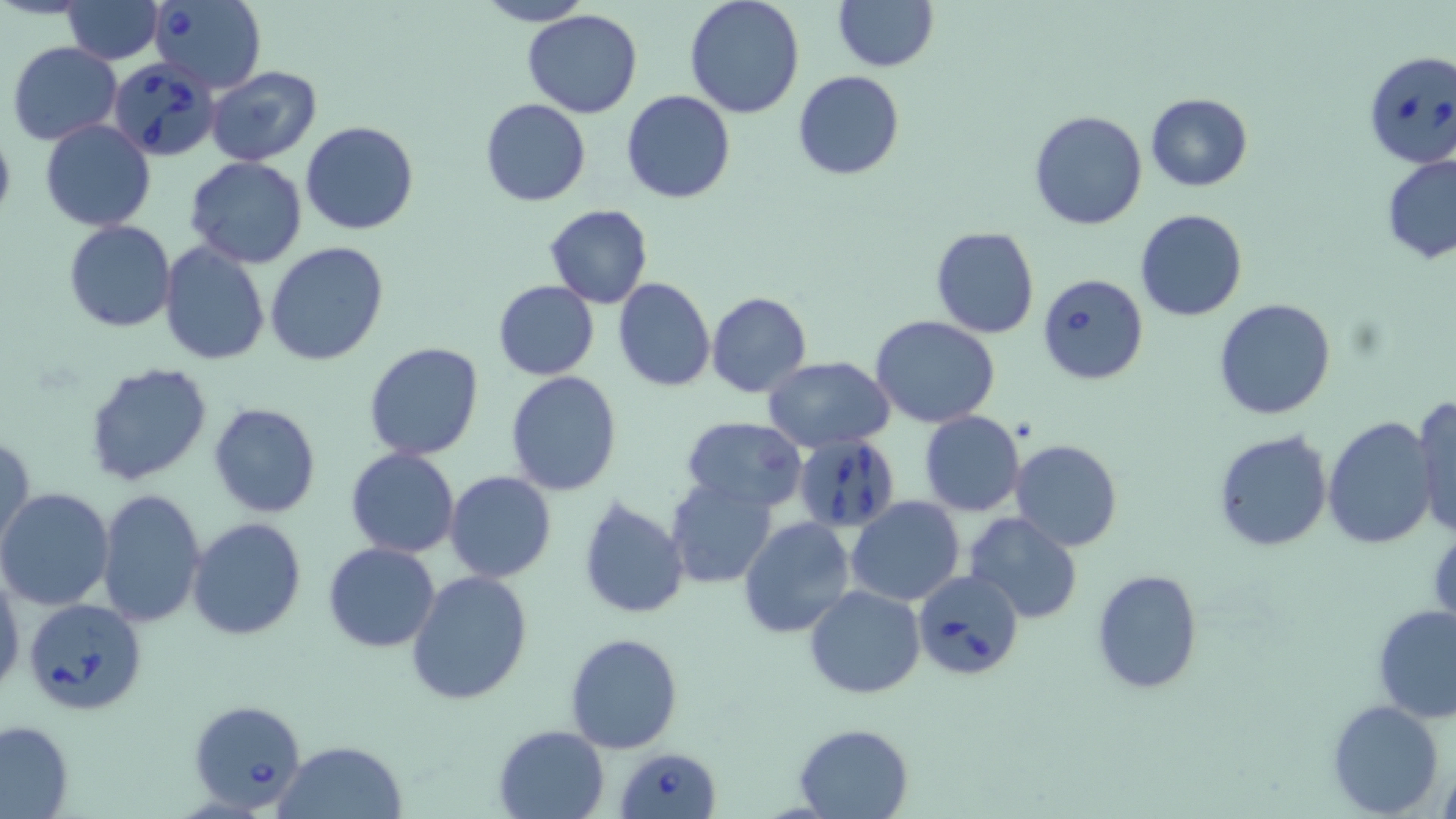
Summary:
  - Coordinate format: approximate bounding boxes as named x1/y1/x2/y2 corners in pixels
  - Uninfected red blood cell locations: (x1=62, y1=0, x2=163, y2=62), (x1=683, y1=0, x2=807, y2=119), (x1=832, y1=0, x2=938, y2=72), (x1=475, y1=1, x2=595, y2=26), (x1=521, y1=9, x2=643, y2=119), (x1=8, y1=41, x2=122, y2=145), (x1=206, y1=66, x2=324, y2=165), (x1=792, y1=69, x2=906, y2=180), (x1=621, y1=89, x2=736, y2=204), (x1=1145, y1=93, x2=1253, y2=192), (x1=480, y1=98, x2=590, y2=206), (x1=1028, y1=109, x2=1148, y2=230), (x1=0, y1=117, x2=16, y2=232), (x1=40, y1=119, x2=156, y2=233), (x1=300, y1=121, x2=419, y2=236), (x1=1381, y1=153, x2=1456, y2=265), (x1=186, y1=157, x2=309, y2=271), (x1=544, y1=205, x2=654, y2=307), (x1=1135, y1=209, x2=1248, y2=323), (x1=64, y1=219, x2=177, y2=331), (x1=930, y1=226, x2=1040, y2=339), (x1=60, y1=232, x2=266, y2=350), (x1=264, y1=241, x2=390, y2=367), (x1=158, y1=242, x2=271, y2=368), (x1=613, y1=277, x2=715, y2=392), (x1=493, y1=280, x2=600, y2=380), (x1=706, y1=291, x2=812, y2=398), (x1=1213, y1=299, x2=1337, y2=421), (x1=871, y1=316, x2=1000, y2=427), (x1=363, y1=340, x2=485, y2=460), (x1=762, y1=357, x2=897, y2=452), (x1=84, y1=361, x2=214, y2=486), (x1=505, y1=372, x2=624, y2=496), (x1=1412, y1=396, x2=1456, y2=538), (x1=207, y1=402, x2=322, y2=518), (x1=919, y1=410, x2=1025, y2=516), (x1=1321, y1=415, x2=1437, y2=551), (x1=681, y1=416, x2=808, y2=512), (x1=1212, y1=430, x2=1333, y2=554), (x1=1, y1=432, x2=35, y2=553), (x1=1009, y1=439, x2=1124, y2=552), (x1=345, y1=448, x2=460, y2=559), (x1=443, y1=471, x2=556, y2=583), (x1=665, y1=478, x2=778, y2=588), (x1=0, y1=488, x2=116, y2=611), (x1=98, y1=490, x2=206, y2=629), (x1=577, y1=495, x2=690, y2=619), (x1=846, y1=496, x2=966, y2=605), (x1=964, y1=512, x2=1083, y2=624), (x1=188, y1=518, x2=308, y2=640), (x1=738, y1=518, x2=854, y2=639), (x1=323, y1=542, x2=441, y2=652), (x1=0, y1=568, x2=23, y2=702), (x1=406, y1=569, x2=532, y2=706), (x1=1092, y1=569, x2=1203, y2=693), (x1=805, y1=586, x2=926, y2=698), (x1=1372, y1=603, x2=1456, y2=723), (x1=564, y1=631, x2=682, y2=753), (x1=1327, y1=700, x2=1444, y2=817), (x1=0, y1=720, x2=74, y2=818), (x1=793, y1=722, x2=916, y2=818), (x1=492, y1=724, x2=610, y2=819), (x1=274, y1=739, x2=408, y2=818), (x1=1438, y1=758, x2=1456, y2=819)
  - Babesia divergens-infected red blood cell locations: (x1=149, y1=1, x2=267, y2=91), (x1=1361, y1=48, x2=1456, y2=169), (x1=109, y1=55, x2=219, y2=161), (x1=1037, y1=273, x2=1148, y2=385), (x1=795, y1=436, x2=901, y2=531), (x1=912, y1=569, x2=1024, y2=679), (x1=25, y1=599, x2=149, y2=717), (x1=185, y1=698, x2=306, y2=813), (x1=616, y1=747, x2=719, y2=819)
  - Slide-level diagnosis: Babesia divergens
  - Magnification: 1000x
  - Field of view: one of a larger specimen
  - Modality: optical microscopy
  - Preparation: thin blood smear
  - Stain: May-Grünwald-Giemsa
  - Image size: 1456×819 pixels